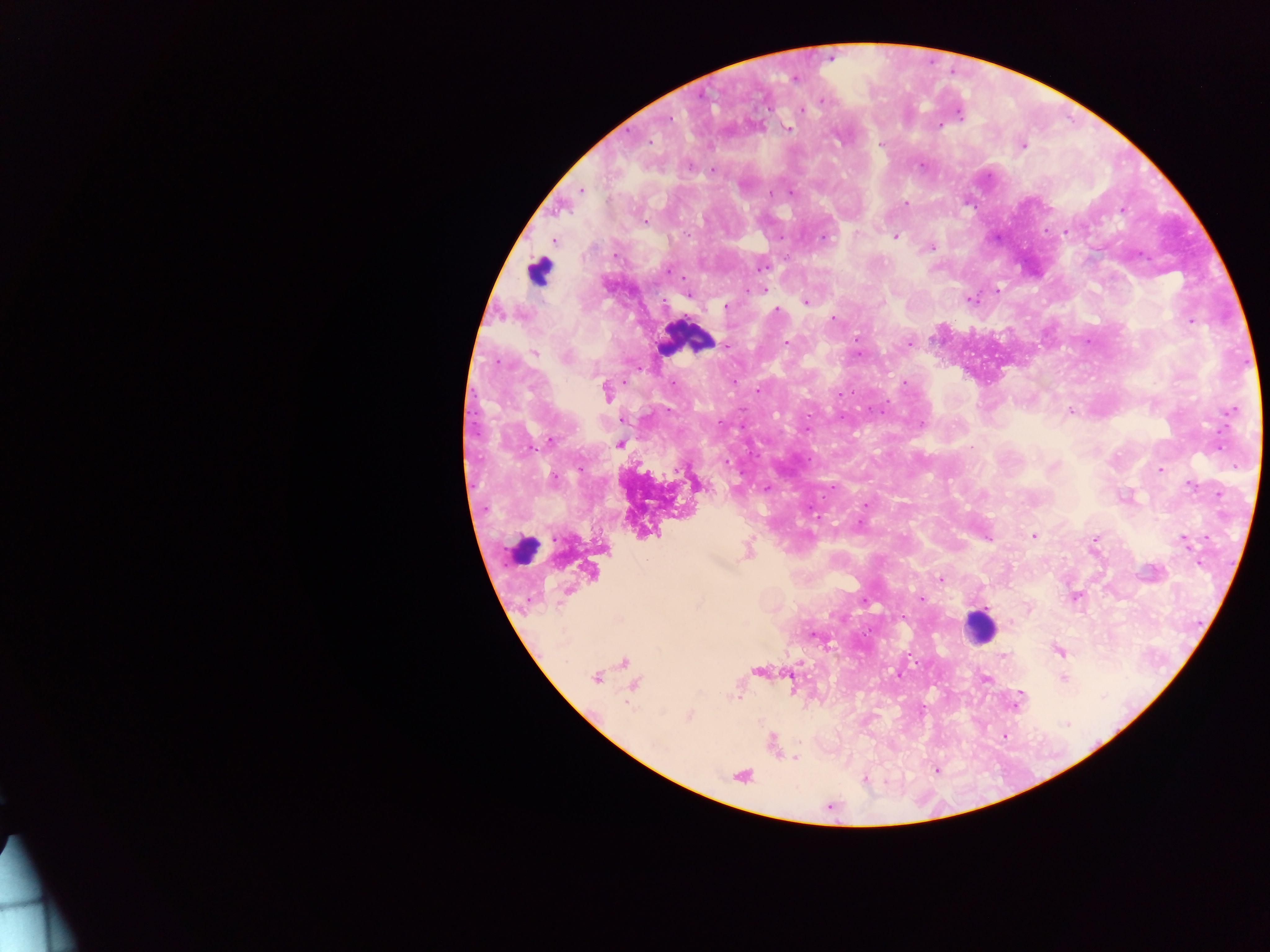
{
  "country": "Ghana",
  "leukocyte_locations": "approximate centers as x y in pixels: 539 271; 686 338; 523 550; 978 627",
  "image_size": "1270×952 pixels",
  "preparation": "thick blood film",
  "field_of_view": "single",
  "capture": "mobile-phone photograph through a microscope",
  "malaria_parasite_locations": "approximate centers as x y in pixels: 795 77; 822 99; 801 110; 788 129; 649 141; 881 145; 1022 145; 921 166; 711 169; 581 190; 772 193; 905 203; 1122 210; 645 221; 1065 232; 895 236; 553 240; 930 247; 760 265; 669 270; 763 289; 996 289; 688 294; 968 299; 806 302; 725 306; 832 318; 1191 322; 725 343; 908 343; 535 352; 858 353; 904 384; 759 390; 606 391; 838 394; 1231 410; 1070 411; 623 419; 921 424; 619 443; 971 448; 1053 466; 1160 469; 1190 484; 697 485; 765 486; 1219 495; 865 505; 1033 535; 1095 539; 1184 541; 748 551; 1200 562; 941 579; 1076 597; 922 598; 1027 607; 903 615; 813 634; 1058 650; 1004 656; 624 662; 758 671; 899 674; 596 677; 1064 677; 984 678; 633 684; 1019 696; 1015 703; 688 716; 1003 735; 795 757; 935 770; 741 775; 865 779"
}